Describe the morphology of the erythrocytes.
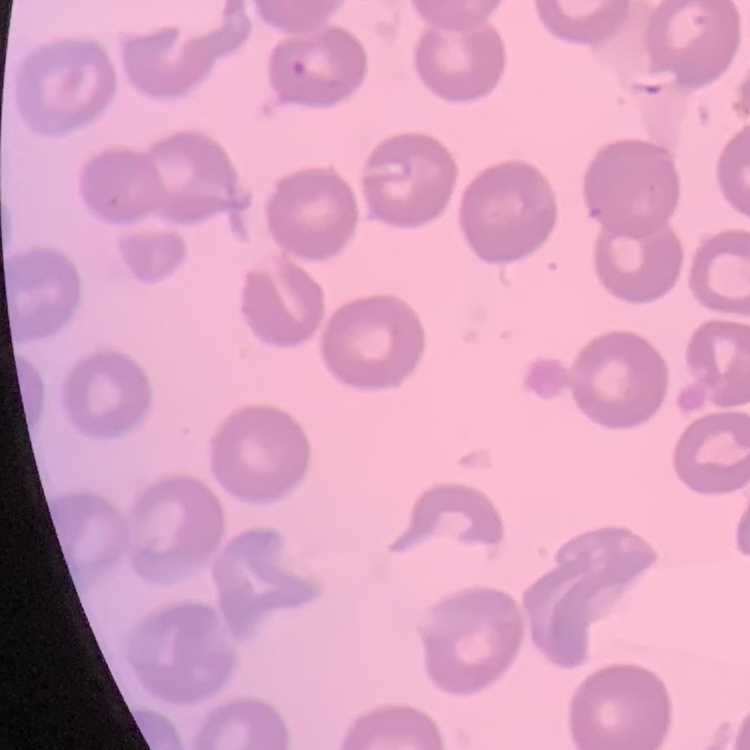
They show no rouleaux formation.

Summary:
  - Preparation: thin peripheral smear
  - Stain: Field's or Giemsa
  - Image type: square crop of a larger photomicrograph